Assess this cell for malaria.
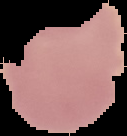
It is uninfected.

image size = 127×136 pixels
preparation = thin blood film
image type = segmented cell region with the area outside set to black